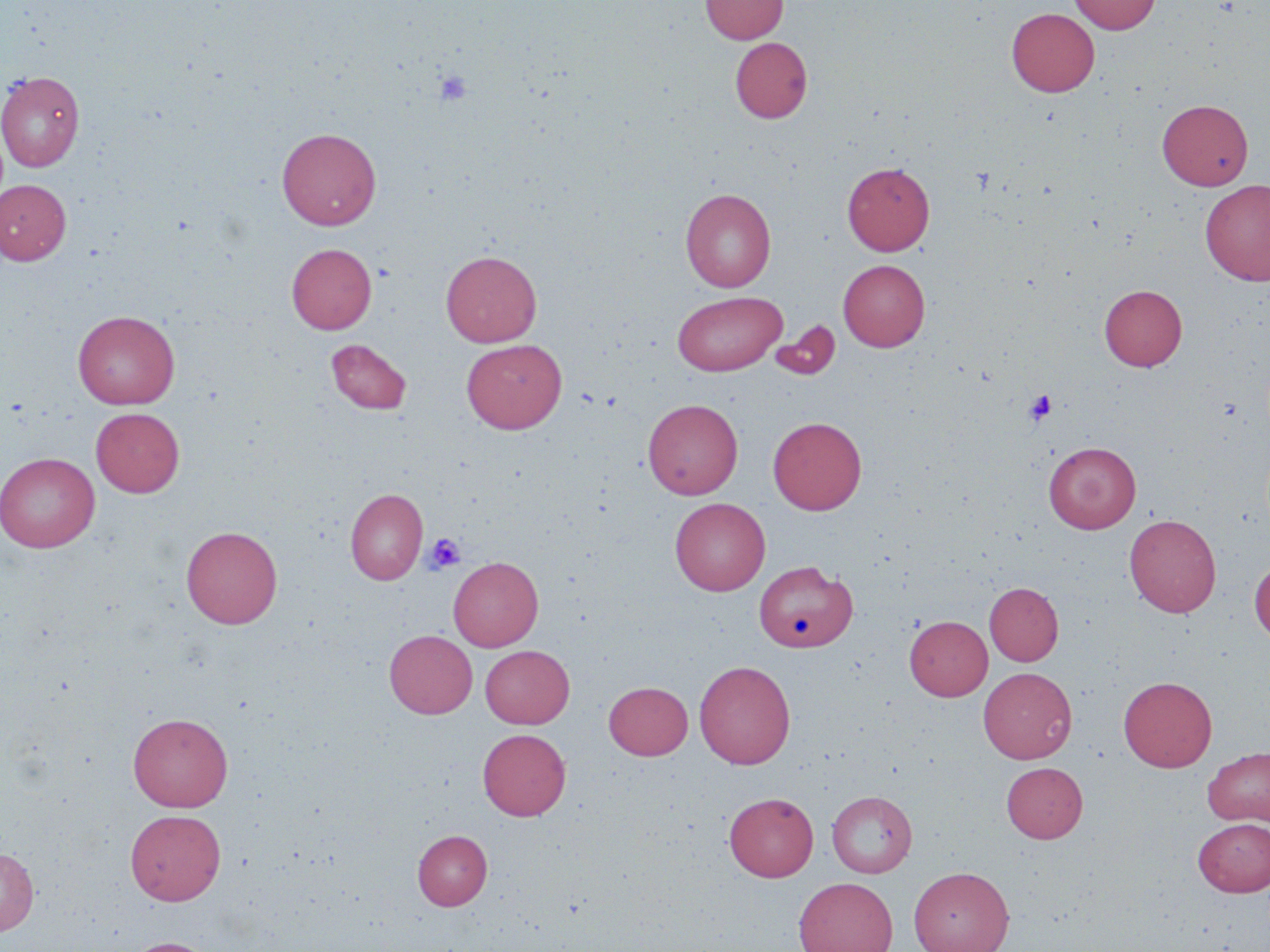

Summary:
  - Coordinate format: approximate bounding boxes as (x1, y1, x2, y2) in pixels
  - Platelet locations: (434, 70, 472, 106), (1024, 389, 1057, 425), (425, 534, 466, 572)
  - Uninfected red blood cell locations: (701, 0, 788, 44), (1068, 0, 1161, 34), (1006, 8, 1100, 97), (730, 36, 812, 123), (0, 71, 85, 171), (1157, 99, 1253, 190), (277, 127, 381, 229), (842, 161, 935, 255), (0, 179, 71, 265), (1200, 180, 1270, 285), (680, 188, 776, 291), (287, 243, 376, 334), (440, 250, 542, 347), (838, 259, 930, 351), (1099, 284, 1187, 371), (672, 291, 787, 376), (73, 310, 180, 409), (770, 319, 840, 380), (326, 338, 412, 415), (461, 338, 567, 434), (643, 398, 743, 499), (91, 407, 185, 497), (768, 416, 866, 515), (1043, 442, 1141, 533), (0, 452, 100, 553), (345, 488, 427, 584), (670, 497, 770, 595), (1124, 514, 1221, 617), (181, 526, 283, 628), (448, 556, 543, 651), (1249, 557, 1270, 644), (754, 560, 857, 652), (984, 582, 1063, 666), (904, 616, 992, 700), (384, 630, 477, 718), (480, 645, 574, 728), (694, 660, 795, 768), (978, 667, 1077, 763), (1119, 675, 1217, 772), (604, 681, 693, 760), (128, 712, 233, 811), (478, 728, 571, 821), (1202, 746, 1270, 826), (1001, 762, 1088, 842), (827, 790, 917, 877), (724, 792, 818, 881), (125, 809, 226, 905), (1193, 817, 1270, 896), (412, 830, 492, 910), (0, 847, 38, 936), (908, 865, 1014, 952), (793, 876, 899, 952), (122, 937, 220, 952)
  - Slide-level diagnosis: negative for blood parasites
  - Stain: May-Grünwald-Giemsa
  - Image size: 1270×952 pixels
  - Magnification: 1000x
  - Field of view: single
  - Modality: optical microscopy
  - Preparation: thin blood film